Point out each Plasmodium parasite.
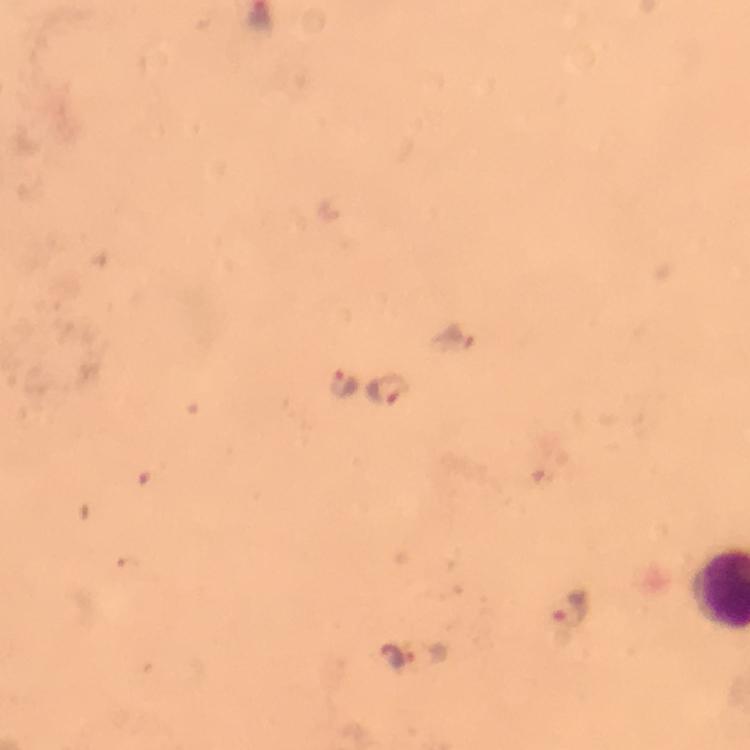
Approximate centers as (x, y) in pixels.
Plasmodium parasites: (344, 385), (387, 389), (569, 612), (391, 655).

context = from a diagnostic examination for malaria
preparation = thick blood film
capture = smartphone camera through the microscope
immersion oil = used
cropped from = one field of view
magnification = 100x
image size = 750×750 pixels
stain = Giemsa